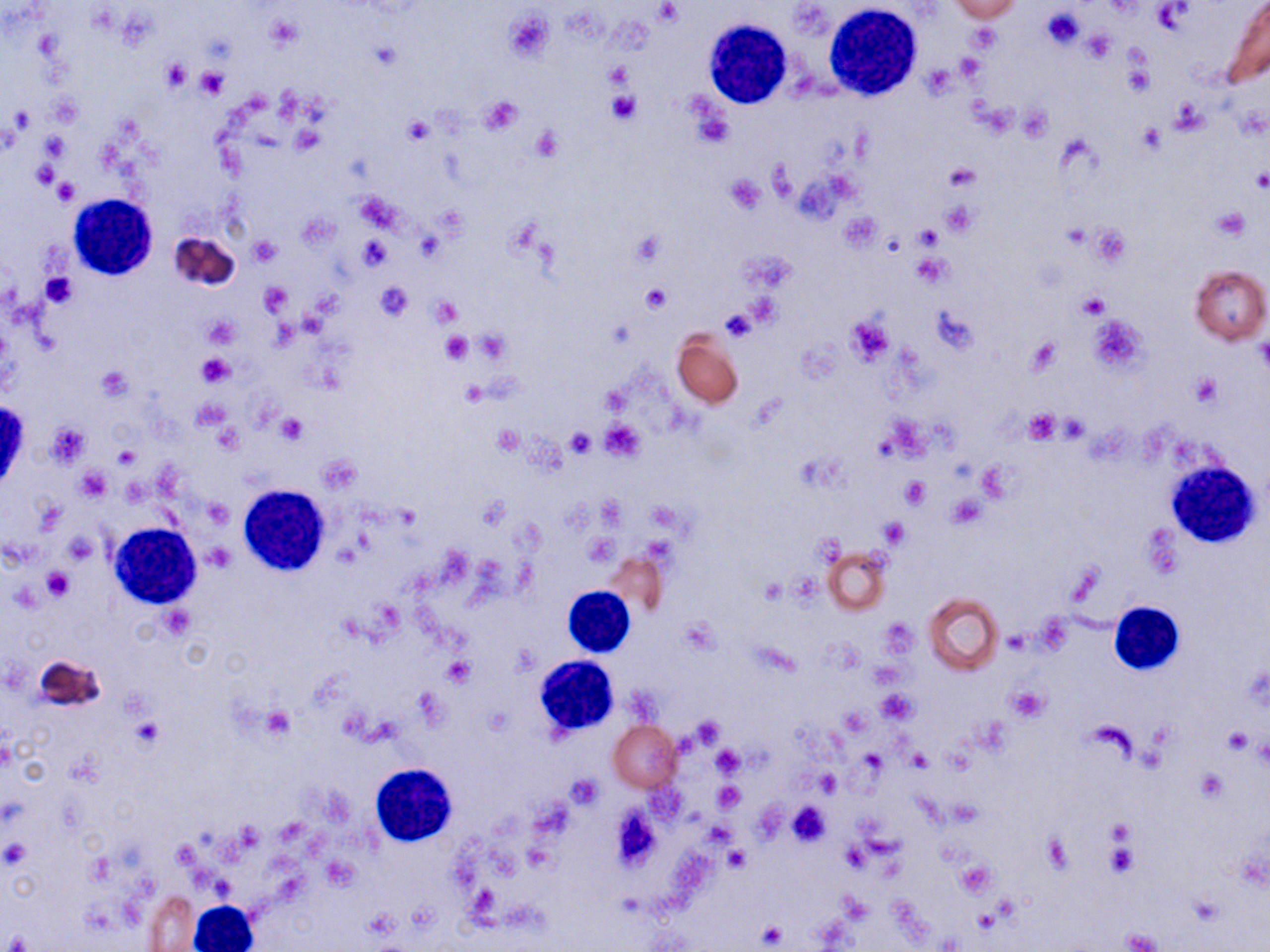
Summary:
  - Coordinate format: approximate bounding boxes as (x1, y1, x2, y2) in pixels
  - Uninfected red blood cell locations: (947, 1, 1024, 22), (1223, 2, 1270, 86), (167, 232, 242, 294), (1190, 265, 1269, 345), (671, 331, 745, 407), (823, 545, 890, 616), (602, 552, 667, 617), (923, 591, 1004, 675), (34, 654, 107, 712), (609, 721, 681, 792), (144, 890, 199, 950)
  - Platelet locations: (1151, 1, 1195, 36), (654, 2, 682, 25), (1041, 6, 1086, 50), (503, 9, 553, 63), (1083, 27, 1115, 63), (370, 43, 401, 71), (954, 51, 986, 83), (160, 58, 190, 93), (603, 62, 634, 90), (924, 65, 954, 99), (195, 67, 227, 99), (607, 90, 640, 124), (477, 97, 524, 135), (402, 116, 433, 145), (290, 124, 323, 153), (531, 127, 562, 161), (944, 166, 979, 193), (1250, 168, 1270, 190), (725, 174, 767, 213), (53, 179, 79, 206), (355, 192, 403, 233), (1212, 207, 1248, 241), (913, 223, 942, 250), (1089, 226, 1128, 266), (250, 235, 281, 265), (358, 236, 391, 271), (912, 254, 952, 287), (42, 273, 78, 308), (374, 281, 414, 321), (640, 281, 670, 313), (259, 282, 290, 317), (1078, 291, 1112, 318), (431, 297, 461, 327), (719, 309, 758, 343), (1089, 315, 1146, 371), (203, 316, 240, 349), (846, 317, 893, 364), (440, 330, 473, 364), (474, 330, 509, 363), (1256, 333, 1270, 374), (1023, 338, 1061, 376), (195, 352, 235, 387), (96, 367, 131, 402), (1189, 374, 1221, 407), (459, 383, 487, 407), (1023, 409, 1060, 444), (278, 414, 307, 445), (1057, 416, 1089, 443), (599, 418, 647, 462), (47, 424, 88, 467), (492, 427, 522, 456), (567, 428, 596, 457), (112, 446, 141, 470), (75, 469, 110, 501), (902, 475, 930, 508), (203, 498, 231, 528), (879, 520, 908, 547), (64, 534, 98, 564), (582, 534, 615, 565), (206, 543, 234, 571), (44, 568, 74, 599), (760, 577, 787, 605), (442, 657, 474, 687), (1005, 686, 1049, 722), (877, 690, 915, 724), (260, 707, 296, 740), (134, 718, 162, 751), (1223, 729, 1252, 755), (711, 746, 743, 778), (814, 770, 842, 795), (1197, 771, 1226, 801), (566, 775, 602, 809), (714, 783, 744, 810), (787, 801, 831, 845), (3, 841, 29, 866), (724, 847, 749, 872), (958, 862, 995, 896), (758, 922, 786, 947), (1120, 928, 1163, 952)
  - White blood cell locations: (822, 4, 924, 101), (705, 18, 793, 109), (68, 193, 157, 280), (1167, 459, 1258, 548), (237, 483, 330, 577), (109, 523, 201, 609), (563, 587, 635, 657), (1109, 602, 1184, 674), (534, 655, 618, 737), (369, 764, 457, 848), (189, 900, 261, 952)
  - Slide-level diagnosis: no evidence of blood parasites
  - Modality: light microscopy
  - Preparation: thin blood film
  - Stain: May-Grünwald-Giemsa
  - Image size: 1270×952 pixels
  - Field of view: single
  - Magnification: 1000x